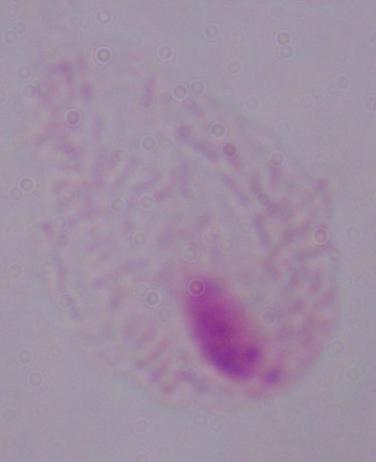

Summary:
  - Modality: photomicrograph
  - Identification: trichomonad
  - Magnification: 1000x